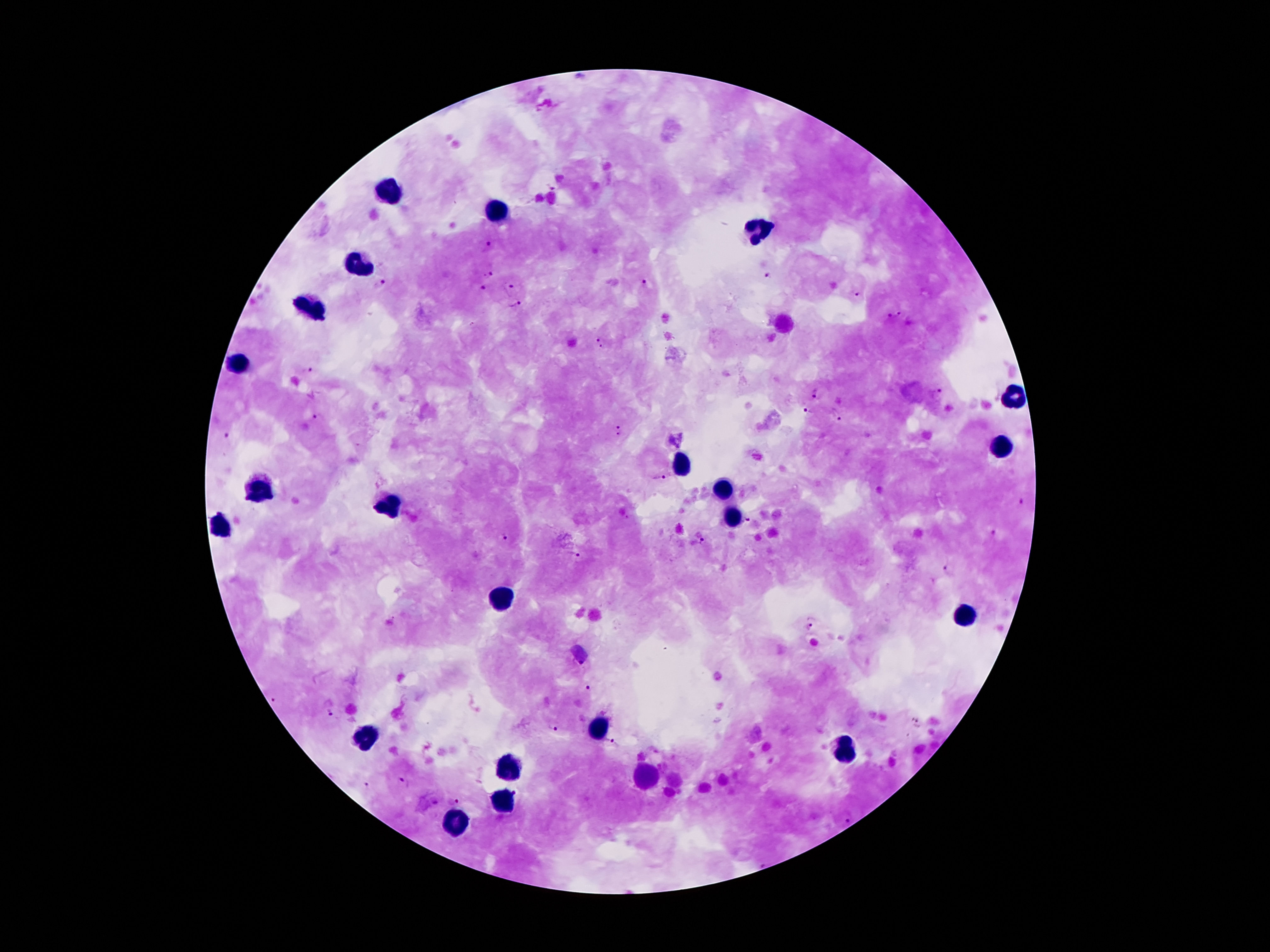
coordinate format = approximate centers as [x, y] in pixels
leukocyte locations = [387, 194], [494, 211], [756, 227], [362, 263], [316, 306], [240, 364], [1012, 394], [998, 446], [679, 466], [723, 488], [255, 490], [391, 505], [733, 515], [221, 528], [504, 597], [968, 614], [597, 727], [364, 739], [844, 748], [509, 770], [649, 776], [507, 798], [458, 821]
Plasmodium parasite locations = [488, 245], [487, 274], [768, 275], [383, 282], [645, 282], [508, 285], [482, 288], [858, 297], [515, 305], [893, 315], [600, 343], [305, 370], [813, 393], [937, 394], [808, 411], [835, 413], [318, 416], [618, 430], [228, 439], [657, 477], [1022, 500], [747, 521], [997, 532], [502, 536], [702, 541], [572, 553], [949, 568], [813, 625], [581, 665], [589, 689], [275, 700], [330, 714], [917, 721], [551, 727], [612, 743], [404, 783], [365, 784], [454, 800], [848, 819], [761, 861]
magnification = 100x
image size = 1270×952 pixels
patient malaria status = infected with Plasmodium falciparum
field of view = one from this slide
capture = smartphone camera through the microscope eyepiece
stain = Giemsa
preparation = thick blood smear